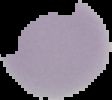

Summary:
  - Preparation: thin blood smear
  - Image size: 112×100 pixels
  - Image type: segmented cell region with the area outside set to black
  - Malaria status: uninfected